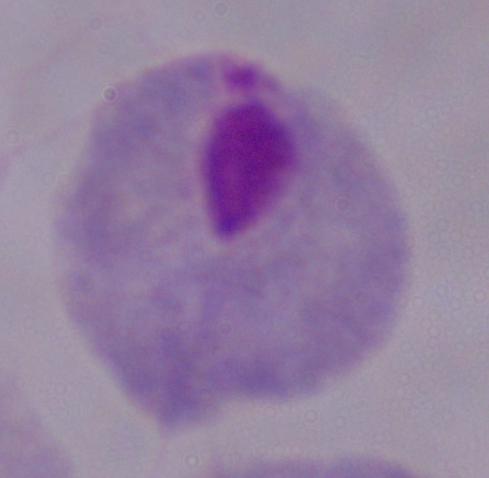 1000x magnification. Micrograph. A trichomonad is seen.